Locate every blood parasite and identify its species.
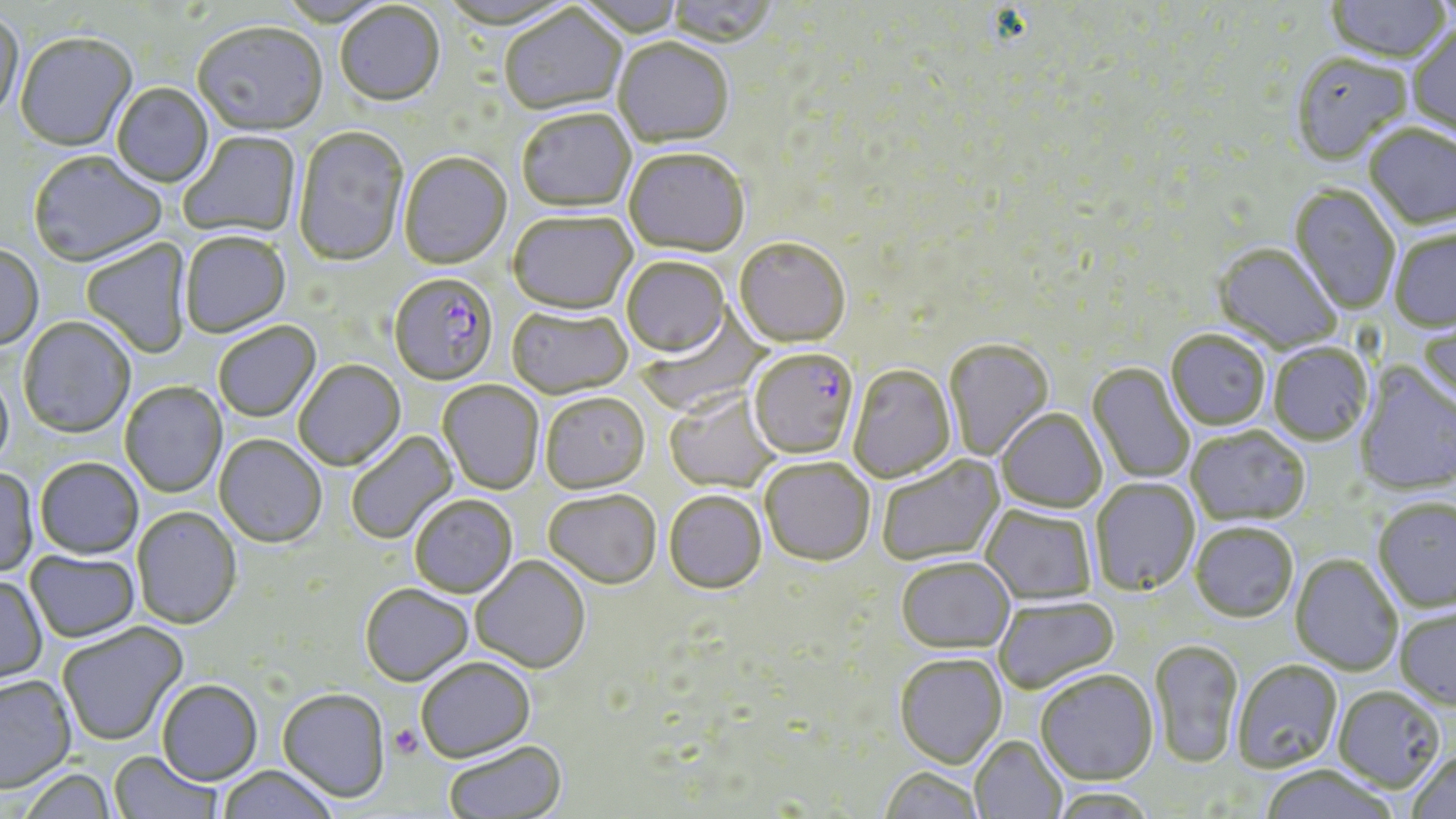

Approximate bounding boxes as [x1, y1, x2, y2] in pixels.
Plasmodium falciparum-infected red blood cells: [390, 275, 498, 387], [748, 349, 861, 462].
No Plasmodium ovale, Plasmodium malariae, Plasmodium vivax, Babesia divergens, or Trypanosoma brucei observed.

slide_level_diagnosis: Plasmodium falciparum
magnification: 1000x
stain: May-Grünwald-Giemsa
preparation: thin blood smear
image_size: 1456×819 pixels
platelet_locations: 'approximate bounding boxes as [x1, y1, x2, y2] in pixels: [388, 724, 423, 759]'
uninfected_red_blood_cell_locations: 'approximate bounding boxes as [x1, y1, x2, y2] in pixels: [573, 0, 687, 40], [665, 0, 778, 51], [438, 1, 579, 34], [1324, 1, 1453, 63], [275, 2, 398, 28], [335, 4, 446, 109], [499, 7, 626, 118], [0, 11, 26, 122], [192, 24, 328, 139], [1407, 25, 1456, 141], [14, 34, 139, 154], [613, 40, 734, 150], [1290, 55, 1413, 165], [112, 84, 214, 189], [517, 111, 636, 215], [1364, 125, 1456, 230], [293, 128, 409, 268], [179, 132, 301, 239], [623, 151, 750, 259], [28, 153, 168, 269], [399, 154, 512, 272], [1289, 185, 1401, 314], [508, 214, 638, 317], [1389, 229, 1456, 332], [181, 234, 291, 339], [81, 239, 193, 359], [734, 240, 851, 350], [1213, 243, 1342, 353], [0, 245, 44, 352], [621, 259, 730, 360], [631, 300, 783, 416], [507, 307, 632, 400], [1418, 314, 1456, 413], [18, 317, 136, 439], [213, 323, 322, 423], [1166, 330, 1271, 430], [943, 340, 1055, 463], [1268, 343, 1373, 445], [294, 361, 406, 472], [1087, 363, 1195, 485], [1355, 364, 1455, 496], [847, 366, 957, 484], [0, 368, 14, 474], [437, 381, 544, 496], [120, 382, 227, 498], [665, 389, 781, 494], [540, 395, 650, 495], [996, 409, 1107, 514], [1186, 425, 1311, 526], [346, 430, 460, 545], [214, 436, 327, 549], [877, 455, 1006, 567], [35, 459, 143, 560], [760, 459, 875, 568], [0, 469, 39, 578], [1090, 478, 1200, 596], [544, 492, 661, 591], [664, 493, 767, 597], [410, 496, 518, 599], [1373, 498, 1456, 612], [980, 505, 1097, 606], [132, 507, 242, 630], [1189, 522, 1298, 623], [25, 551, 140, 643], [1290, 553, 1403, 676], [471, 558, 591, 675], [895, 558, 1015, 655], [0, 577, 48, 687], [360, 586, 474, 688], [994, 596, 1119, 694], [1395, 606, 1456, 710], [57, 623, 189, 748], [1149, 640, 1243, 769], [894, 656, 1007, 769], [416, 660, 536, 765], [1231, 660, 1343, 774], [1034, 670, 1159, 786], [0, 676, 77, 794], [157, 682, 262, 787], [1333, 686, 1445, 792], [277, 691, 390, 804], [970, 736, 1067, 819], [444, 742, 568, 818], [1407, 749, 1456, 819], [109, 752, 221, 819], [1259, 766, 1400, 819], [217, 767, 339, 819], [879, 768, 984, 819], [19, 771, 117, 819], [1049, 788, 1157, 818]'
modality: light microscopy
field_of_view: single